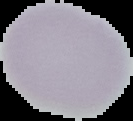

preparation = thin blood smear
image size = 133×121 pixels
result = no malaria parasites detected
image type = segmented cell region with the area outside set to black